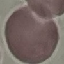 Result: negative for malaria parasites. Thin blood film. Photographed with a smartphone camera at the microscope eyepiece. Cell patch, automatically extracted from a larger field of view and resized to 64 × 64 pixels. Giemsa-stained preparation.